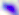 Micrograph. Toxoplasma gondii is seen. Captured at 400x magnification.